State which parasite is depicted.
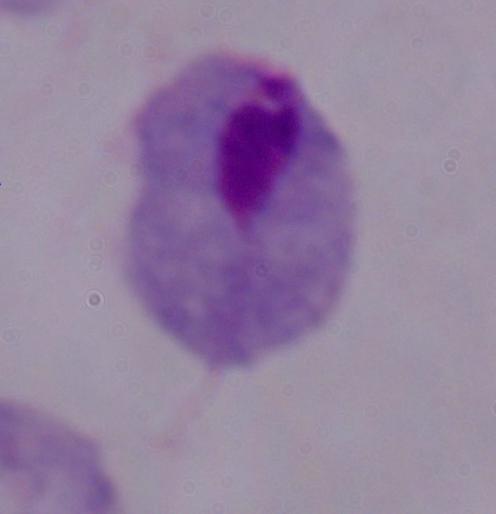
A trichomonad.

Summary:
  - Magnification: 1000x
  - Modality: micrograph